Report the malaria status of this cell.
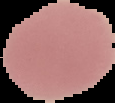

It is uninfected.

preparation = thin blood film
image size = 115×103 pixels
image type = segmented cell region with the area outside set to black